State which parasite is depicted.
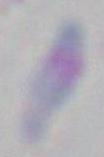

This is Toxoplasma gondii.

Summary:
  - Modality: micrograph
  - Magnification: 1000x